Report the malaria status of this cell.
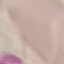

It is uninfected.

Summary:
  - Preparation: thin smear
  - Image type: automatically extracted cell patch, resized to 64 × 64 pixels
  - Capture: smartphone through the microscope eyepiece
  - Stain: Giemsa